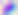

Summary:
  - Modality: micrograph
  - Identification: Toxoplasma gondii
  - Magnification: 400x